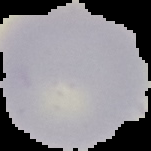

preparation = thin blood film
image type = segmented cell region on a black background
image size = 151×151 pixels
malaria status = uninfected